Assess this cell for malaria.
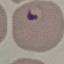
It is parasitized.

Summary:
  - Capture: smartphone camera at the microscope eyepiece
  - Preparation: thin blood smear
  - Stain: Giemsa
  - Image type: cell patch, automatically extracted from a larger field of view and resized to 64 × 64 pixels